Report the malaria status of this cell.
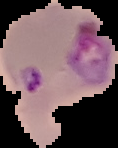

Parasitized.

{
  "preparation": "thin blood smear",
  "image_type": "segmented cell region on a black background",
  "image_size": "118×148 pixels"
}